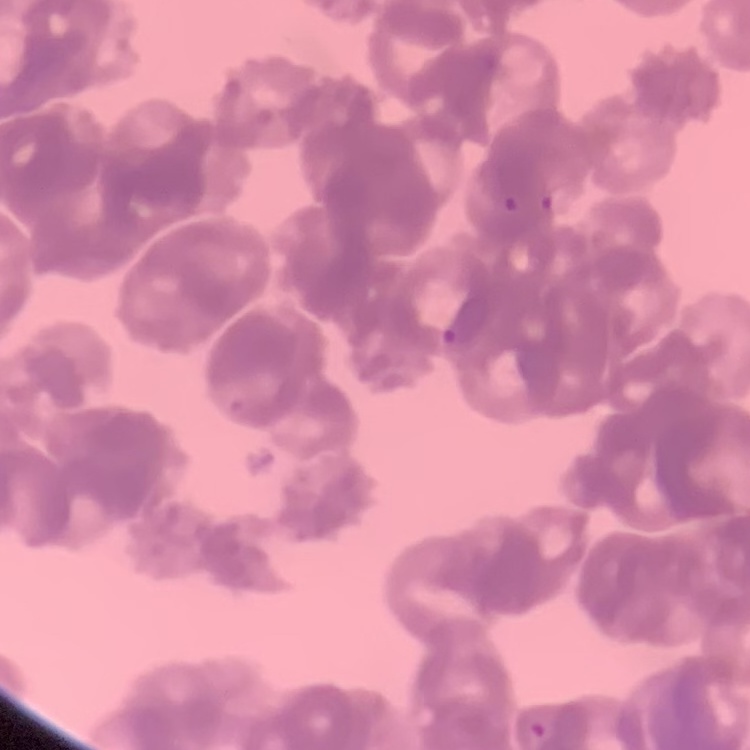

Summary:
  - Erythrocyte morphology: rouleaux formation
  - Image type: one tile cut from a larger photomicrograph
  - Stain: Field's or Giemsa
  - Preparation: thin blood smear